Report the malaria status of this cell.
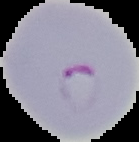

It is parasitized.

Image is 139×142 pixels. Cell region segmented out of the field of view; the surrounding area is masked to black. From a thin blood film.